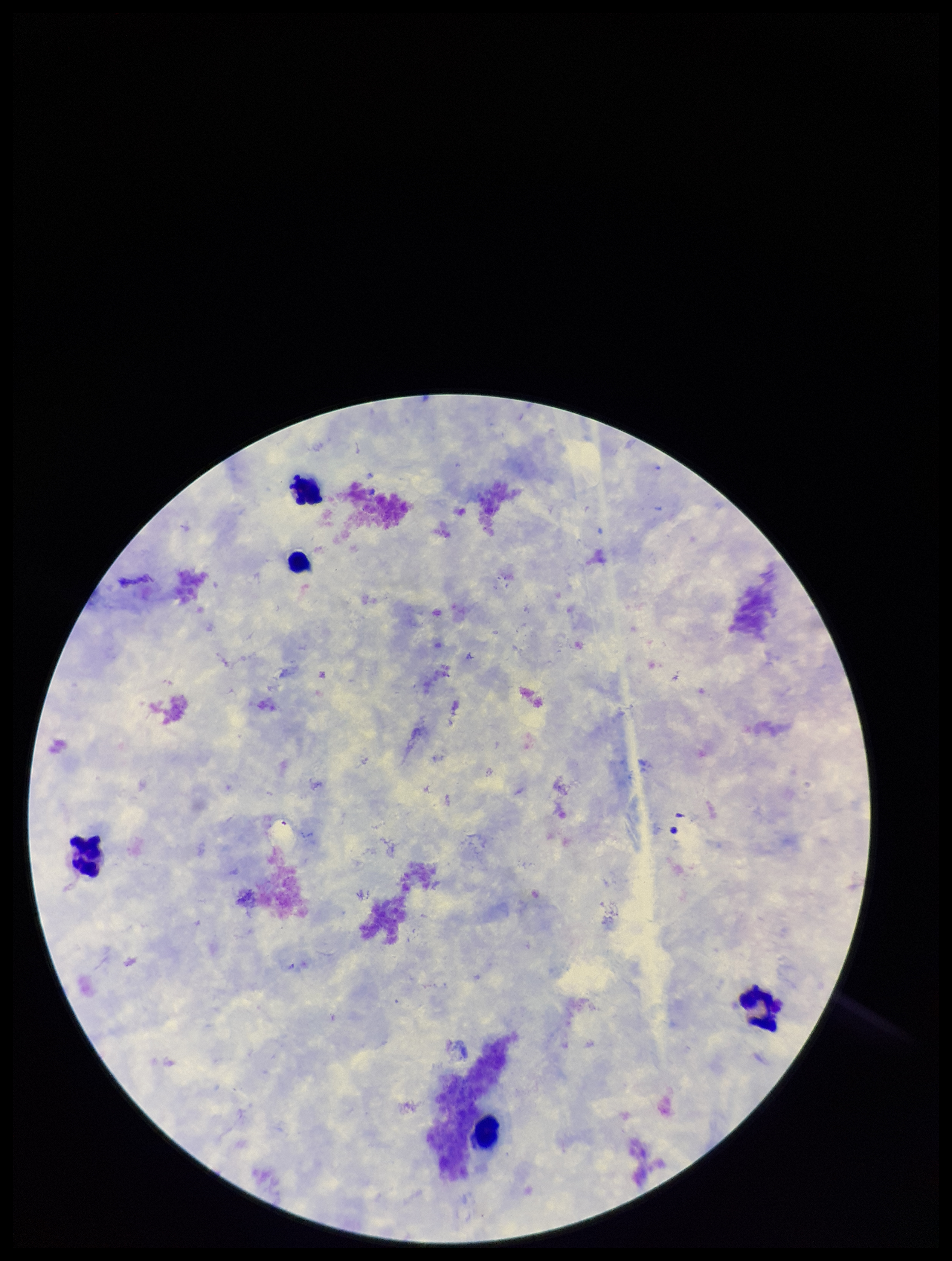
image_size: 952×1261 pixels
preparation: thick smear
plasmodium_parasites: none identified
parasite_count: 0
stain: Giemsa
field_of_view: one from this slide
patient_malaria_status: negative
leukocyte_count: 5
capture: smartphone photograph through the microscope eyepiece